Identify the parasite.
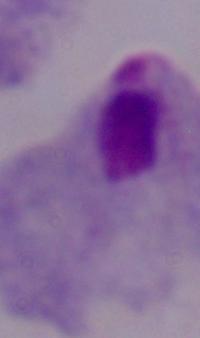
A trichomonad.

{
  "modality": "photomicrograph",
  "magnification": "1000x"
}